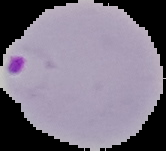

result = malaria parasites detected
preparation = thin blood smear
image type = cell region segmented out of the field of view; surrounding area masked to black
image size = 166×151 pixels